Classify this cell by malaria status.
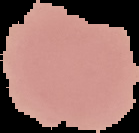
It is uninfected.

Image is 139×133 pixels. From a thin blood film. Segmented cell region on a black background.